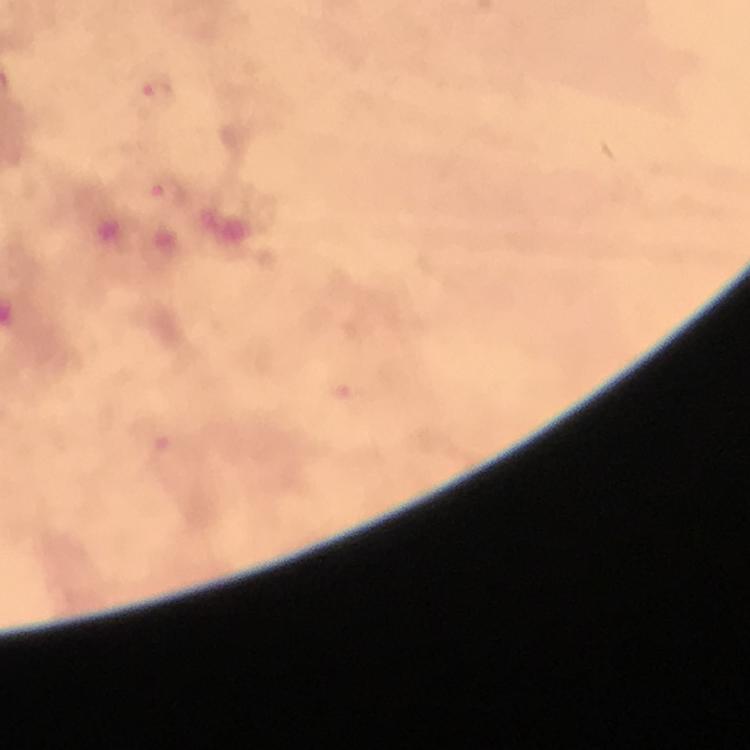
Approximate centers as (x, y) in pixels.
Summary:
  - Malaria parasite locations: (158, 92), (169, 193)
  - Capture: smartphone photograph through a microscope
  - Context: from a malaria diagnostic workup
  - Magnification: 100x
  - Immersion oil: used
  - Preparation: thick smear
  - Image size: 750×750 pixels
  - Stain: Giemsa
  - Cropped from: a single field of view